Name the cell type shown.
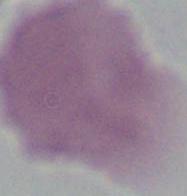
This is an erythrocyte.

Captured at 1000x magnification. Micrograph.